Give the extent of all Plasmodium falciparum-infected red blood cells.
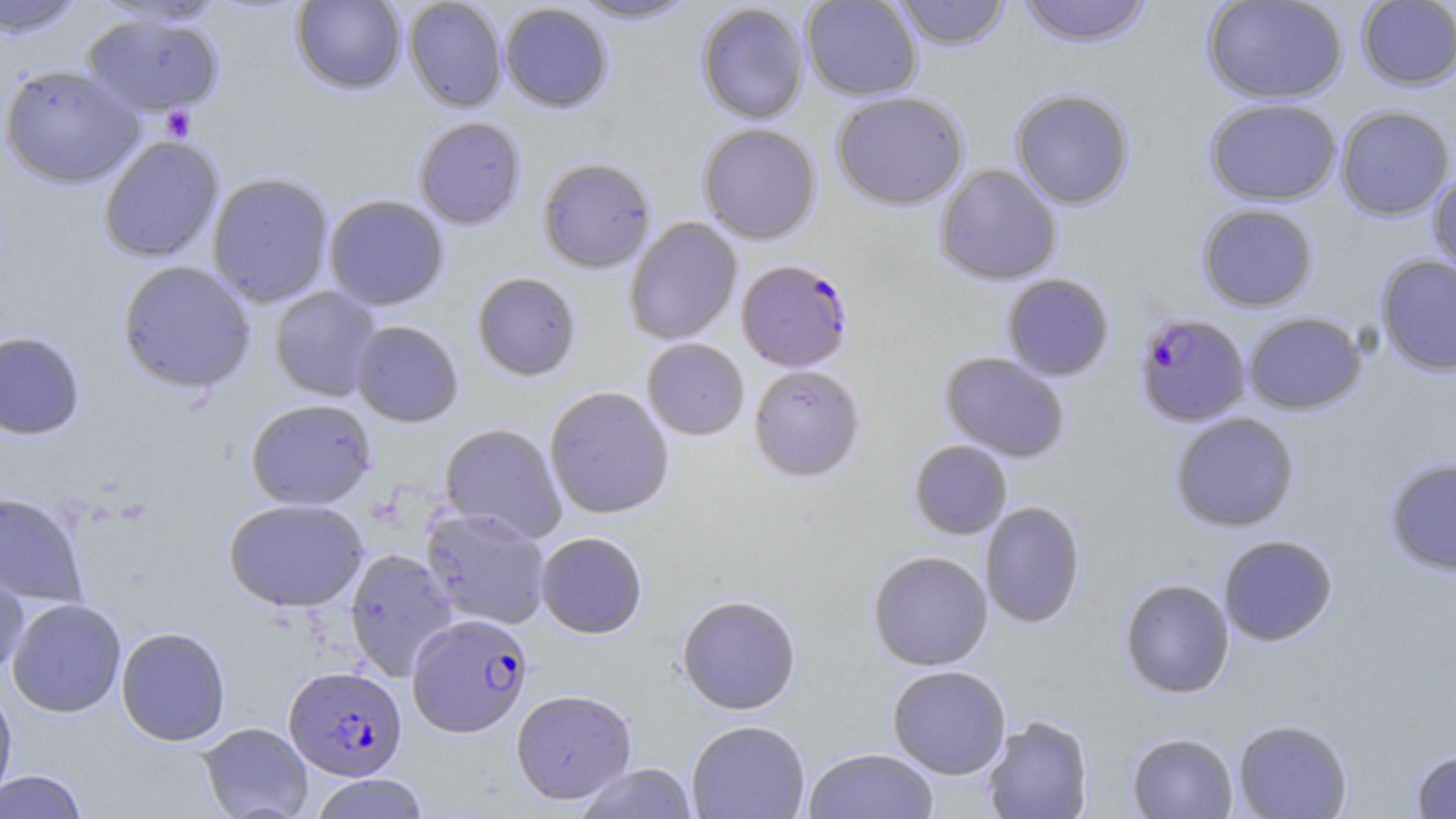

Approximate bounding boxes as (x1, y1, x2, y2) in pixels.
Plasmodium falciparum-infected red blood cells: (736, 259, 854, 373), (1134, 311, 1252, 427), (407, 612, 534, 738), (283, 666, 407, 781).

slide_level_diagnosis: Plasmodium falciparum
modality: optical microscopy
stain: May-Grünwald-Giemsa
image_size: 1456×819 pixels
uninfected_red_blood_cell_locations: 'approximate bounding boxes as (x1, y1, x2, y2) in pixels: (0, 0, 88, 38), (290, 0, 407, 95), (403, 0, 507, 112), (571, 0, 699, 25), (801, 0, 923, 101), (892, 0, 1012, 50), (1016, 0, 1153, 48), (1201, 0, 1348, 105), (1356, 1, 1456, 90), (499, 2, 613, 113), (696, 3, 810, 125), (81, 12, 226, 118), (0, 64, 144, 188), (1010, 89, 1135, 210), (831, 91, 969, 210), (1204, 98, 1342, 206), (1335, 105, 1455, 221), (413, 117, 527, 230), (697, 123, 821, 245), (98, 135, 224, 263), (536, 157, 657, 274), (934, 164, 1062, 286), (1428, 166, 1456, 279), (206, 172, 335, 308), (323, 195, 450, 311), (1197, 203, 1319, 311), (624, 217, 742, 346), (1375, 254, 1456, 376), (116, 260, 256, 394), (472, 272, 581, 382), (1001, 273, 1115, 382), (269, 286, 382, 401), (1242, 311, 1367, 415), (350, 320, 464, 428), (0, 331, 86, 440), (642, 338, 750, 441), (940, 351, 1070, 463), (749, 363, 866, 483), (544, 386, 674, 519), (245, 398, 377, 510), (1169, 412, 1300, 532), (439, 423, 567, 544), (909, 440, 1012, 539), (1383, 457, 1456, 577), (0, 490, 89, 608), (223, 498, 369, 612), (980, 501, 1086, 629), (420, 506, 551, 630), (535, 532, 648, 639), (1218, 534, 1338, 646), (344, 548, 458, 681), (868, 551, 993, 671), (0, 559, 29, 681), (1119, 577, 1235, 699), (676, 594, 801, 715), (7, 598, 127, 718), (116, 626, 231, 746), (887, 665, 1011, 779), (0, 684, 18, 808), (510, 689, 637, 805), (982, 714, 1093, 819), (1233, 718, 1353, 818), (686, 720, 810, 819), (197, 722, 313, 819), (1127, 732, 1238, 818), (803, 747, 939, 819), (1410, 749, 1456, 818), (574, 763, 698, 818), (0, 770, 89, 819), (309, 774, 431, 819)'
preparation: thin blood smear
platelet_locations: 'approximate bounding boxes as (x1, y1, x2, y2) in pixels: (161, 105, 196, 141)'
magnification: 1000x
field_of_view: one of a larger specimen